Identify the parasite.
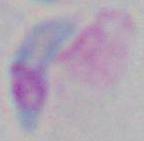
Toxoplasma gondii.

1000x magnification. Micrograph.